Identify the parasite.
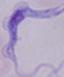

This is a trypanosome.

Summary:
  - Modality: micrograph
  - Magnification: 1000x